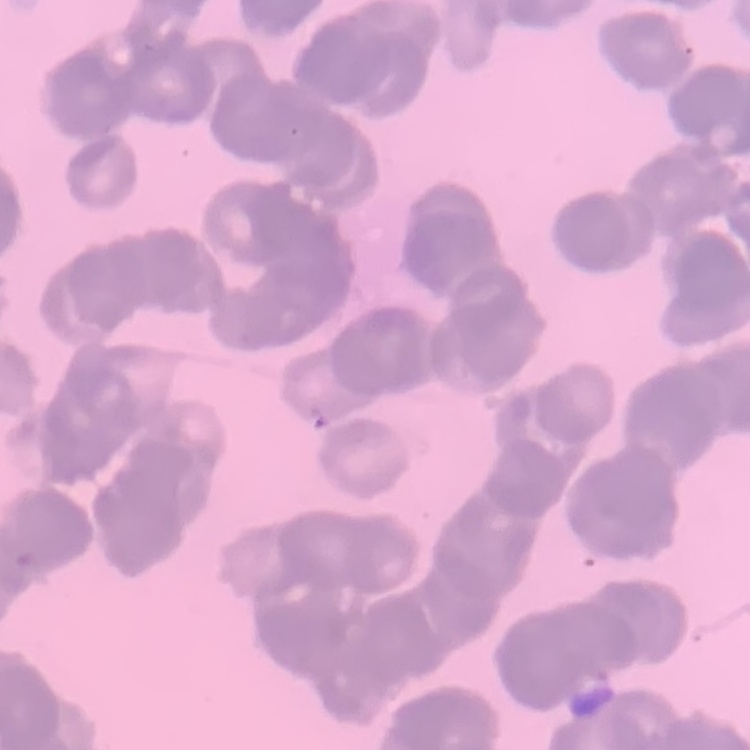
erythrocyte morphology = rouleaux formation
image type = square crop of a larger photomicrograph
stain = Field's or Giemsa
preparation = thin blood smear